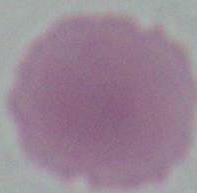
Summary:
  - Magnification: 1000x
  - Modality: micrograph
  - Identification: red blood cell